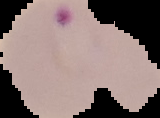
Summary:
  - Malaria status: parasitized
  - Image type: segmented cell region with the area outside set to black
  - Preparation: thin blood smear
  - Image size: 160×118 pixels